Assess this cell for malaria.
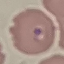

It is parasitized.

capture = smartphone camera at the microscope eyepiece
image type = automatically extracted cell patch, resized to 64 × 64 pixels
stain = Giemsa
preparation = thin smear